Locate and identify every blood parasite.
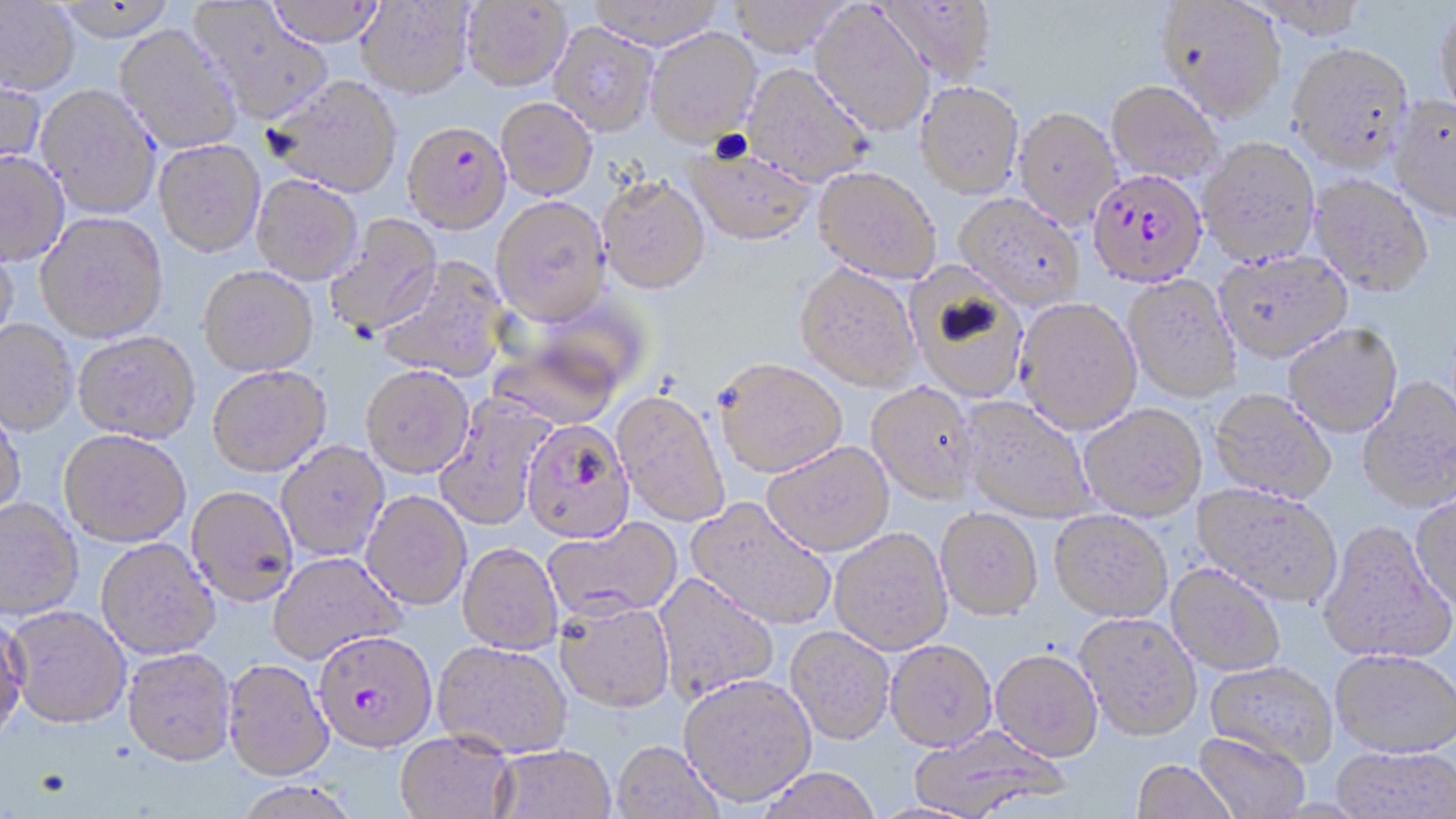
Approximate bounding boxes as (x1, y1, x2, y2) in pixels.
Plasmodium falciparum-infected red blood cells: (403, 120, 511, 232), (1088, 168, 1208, 287), (521, 419, 634, 543), (313, 630, 438, 754).
No Plasmodium ovale, Plasmodium malariae, Plasmodium vivax, Babesia divergens, or Trypanosoma brucei observed.

Uninfected red blood cell locations: (50, 0, 180, 41), (263, 0, 386, 46), (588, 0, 723, 49), (728, 0, 848, 56), (1156, 0, 1287, 120), (0, 1, 81, 96), (191, 1, 333, 125), (356, 1, 473, 98), (462, 1, 571, 91), (876, 1, 997, 85), (1249, 1, 1369, 38), (810, 3, 935, 137), (1435, 4, 1456, 122), (550, 22, 658, 136), (115, 24, 244, 153), (646, 27, 761, 146), (1287, 41, 1414, 173), (742, 63, 873, 186), (0, 75, 46, 179), (266, 75, 402, 197), (915, 80, 1024, 198), (1106, 80, 1223, 185), (37, 84, 162, 219), (1389, 95, 1456, 223), (496, 98, 597, 199), (1014, 106, 1121, 228), (1198, 136, 1320, 266), (154, 139, 265, 257), (685, 148, 816, 246), (0, 151, 70, 267), (813, 165, 943, 284), (251, 174, 362, 284), (1310, 174, 1433, 295), (598, 175, 710, 294), (955, 193, 1085, 309), (490, 195, 612, 325), (36, 212, 168, 342), (325, 215, 443, 338), (0, 241, 19, 349), (1214, 250, 1352, 361), (378, 258, 510, 381), (795, 262, 923, 391), (199, 265, 318, 376), (906, 268, 1031, 404), (1123, 275, 1241, 403), (1015, 297, 1142, 434), (0, 320, 77, 436), (1283, 323, 1402, 437), (74, 331, 200, 443), (487, 331, 628, 431), (714, 358, 847, 477), (208, 365, 331, 476), (361, 365, 474, 478), (1358, 375, 1456, 511), (867, 381, 979, 503), (611, 389, 730, 528), (1209, 389, 1337, 503), (434, 396, 554, 531), (959, 396, 1096, 522), (1078, 403, 1207, 520), (0, 405, 26, 520), (58, 429, 190, 547), (276, 441, 389, 561), (762, 441, 894, 556), (1194, 483, 1343, 606), (187, 486, 298, 606), (362, 491, 471, 610), (1412, 493, 1456, 611), (685, 496, 837, 630), (0, 498, 84, 621), (936, 508, 1042, 620), (1049, 510, 1173, 622), (543, 518, 682, 622), (1318, 520, 1454, 665), (829, 527, 952, 654), (96, 539, 220, 660), (457, 544, 563, 654), (268, 551, 405, 664), (1167, 563, 1286, 675), (654, 573, 780, 705), (554, 599, 675, 711), (7, 606, 132, 729), (0, 612, 30, 747), (1076, 612, 1202, 740), (785, 626, 894, 745), (885, 639, 996, 751), (432, 640, 572, 759), (122, 648, 237, 768), (991, 649, 1102, 761), (1331, 649, 1456, 756), (223, 659, 334, 781), (1205, 661, 1337, 767), (679, 673, 816, 806), (906, 725, 1068, 817), (1194, 731, 1309, 819), (395, 732, 517, 819), (611, 741, 723, 819), (493, 745, 615, 819), (1331, 746, 1456, 819), (1131, 759, 1238, 819), (757, 768, 882, 819), (232, 782, 363, 819). Slide-level diagnosis: Plasmodium falciparum. Thin blood smear. 1000x magnification. One field of a larger specimen. May-Grünwald-Giemsa-stained preparation. Image is 1456×819 pixels. Light microscopy.